State which parasite is depicted.
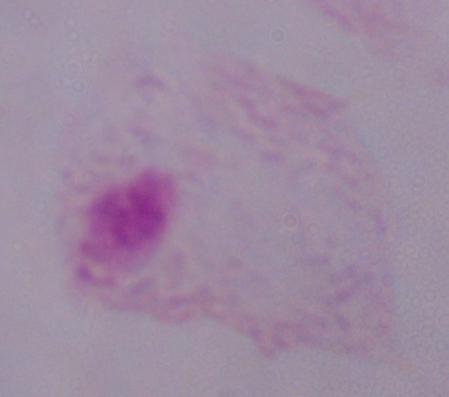

This is a trichomonad.

modality = micrograph
magnification = 1000x